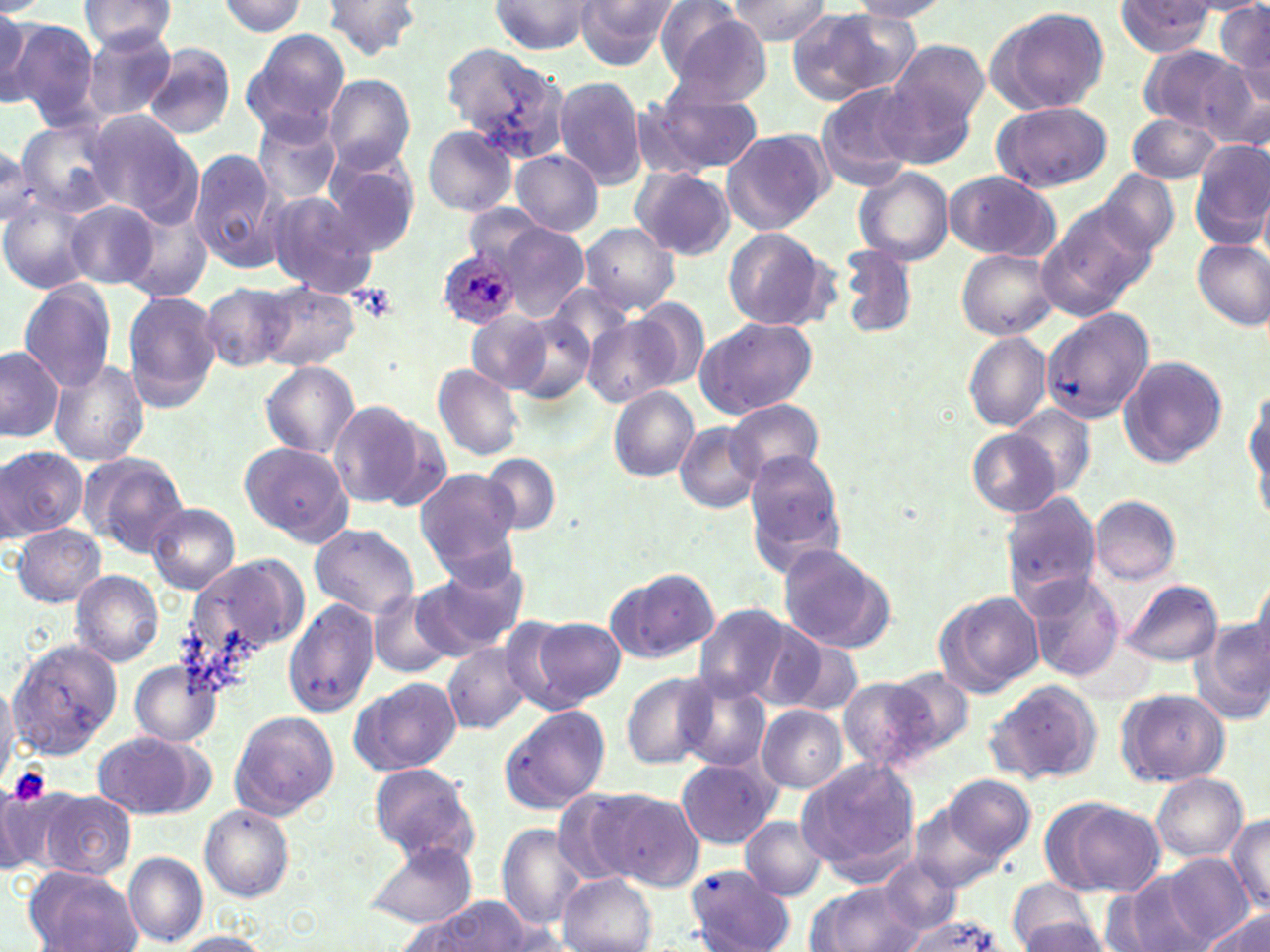
Summary:
  - Coordinate format: approximate bounding boxes as (x1,y1)-(x2,y2) corner pairs in pixels
  - Platelet locations: (7,767)-(50,805)
  - Plasmodium ovale-infected red blood cell locations: (436,251)-(521,330)
  - Uninfected red blood cell locations: (79,0)-(180,55), (573,0)-(676,71), (722,0)-(835,45), (847,0)-(956,20), (1116,0)-(1215,56), (1216,0)-(1270,100), (216,1)-(311,36), (322,1)-(422,59), (488,1)-(602,55), (985,5)-(1110,116), (786,7)-(917,105), (0,8)-(36,110), (662,8)-(772,104), (9,19)-(100,128), (79,27)-(178,122), (242,29)-(350,139), (886,38)-(990,144), (440,42)-(573,163), (141,45)-(237,138), (1138,47)-(1258,139), (322,75)-(415,173), (553,76)-(646,188), (650,81)-(767,174), (815,82)-(922,190), (992,101)-(1111,193), (86,110)-(197,219), (251,111)-(342,205), (1126,111)-(1223,185), (13,115)-(125,217), (422,125)-(517,215), (723,128)-(828,233), (1189,139)-(1270,248), (0,146)-(40,226), (188,148)-(284,277), (511,150)-(603,236), (321,154)-(419,256), (852,167)-(954,266), (631,169)-(737,260), (1096,171)-(1177,258), (943,172)-(1058,259), (264,192)-(378,300), (0,197)-(97,295), (64,199)-(158,287), (1038,199)-(1153,318), (122,201)-(214,302), (489,219)-(590,321), (580,223)-(678,313), (723,227)-(834,329), (1191,239)-(1270,330), (836,246)-(918,340), (957,248)-(1058,340), (18,280)-(118,393), (257,281)-(360,372), (200,282)-(294,372), (549,284)-(636,366), (122,291)-(223,413), (630,297)-(709,390), (1042,303)-(1153,422), (508,310)-(598,405), (468,313)-(553,391), (694,315)-(819,419), (583,316)-(678,408), (963,331)-(1052,431), (0,346)-(62,442), (1116,356)-(1228,468), (48,360)-(150,467), (260,362)-(359,458), (434,364)-(525,461), (1246,380)-(1269,506), (610,386)-(698,480), (329,400)-(430,509), (725,402)-(825,484), (1009,406)-(1097,497), (675,421)-(763,512), (967,429)-(1061,517), (238,440)-(355,547), (0,445)-(85,542), (742,446)-(849,573), (79,451)-(190,557), (480,453)-(560,535), (417,469)-(521,571), (1004,494)-(1102,607), (1090,496)-(1181,585), (146,503)-(241,595), (12,523)-(105,607), (309,525)-(419,619), (775,543)-(895,654), (186,559)-(305,669), (414,562)-(527,658), (72,569)-(165,668), (606,569)-(718,664), (1020,572)-(1122,681), (1121,579)-(1221,666), (368,591)-(453,679), (938,591)-(1044,695), (283,599)-(378,716), (694,603)-(798,704), (527,616)-(624,709), (1190,617)-(1270,726), (771,632)-(863,718), (10,640)-(123,758), (444,643)-(531,733), (129,659)-(220,750), (886,666)-(978,760), (622,673)-(717,769), (0,675)-(21,783), (677,676)-(771,770), (836,676)-(933,773), (350,678)-(462,777), (983,678)-(1104,786), (1116,688)-(1228,788), (759,705)-(848,793), (500,706)-(609,814), (229,710)-(339,820), (92,730)-(211,820), (675,757)-(781,850), (798,758)-(921,876), (368,763)-(477,860), (944,773)-(1035,862), (1152,774)-(1247,863), (0,781)-(70,876), (597,788)-(705,891), (37,789)-(136,880), (549,789)-(645,885), (1052,800)-(1163,898), (198,803)-(294,902), (911,803)-(1004,894), (1225,815)-(1270,911), (739,817)-(827,900), (498,823)-(589,929), (361,840)-(478,929), (123,852)-(209,945), (1163,853)-(1258,948), (872,857)-(963,938), (685,865)-(794,951), (24,866)-(142,952), (557,873)-(657,952), (1113,873)-(1210,952), (1006,881)-(1104,952), (811,882)-(926,951), (406,900)-(548,952), (1198,911)-(1270,952), (899,916)-(1005,952), (1018,918)-(1107,949), (167,931)-(272,951)
  - Slide-level diagnosis: Plasmodium ovale
  - Preparation: thin blood film
  - Image size: 1270×952 pixels
  - Field of view: one of a larger specimen
  - Magnification: 1000x
  - Modality: light microscopy
  - Stain: May-Grünwald-Giemsa